Identify the parasite.
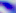
Toxoplasma gondii.

Summary:
  - Magnification: 400x
  - Modality: micrograph